Classify this cell by malaria status.
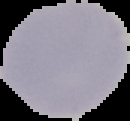

Uninfected.

preparation = thin blood smear
image type = segmented cell region on a black background
image size = 130×121 pixels